Assess this cell for malaria.
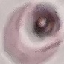

Uninfected.

Cell patch, automatically extracted from a larger field of view and resized to 64 × 64 pixels. Photographed with a smartphone camera at the microscope eyepiece. Giemsa-stained preparation. Thin blood smear.